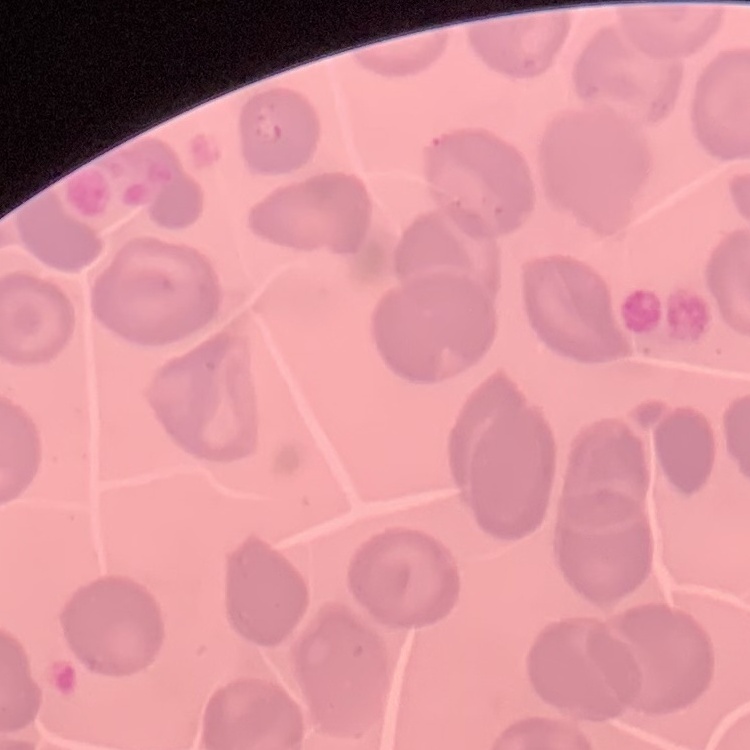 The red blood cells exhibit no rouleaux formation. Thin peripheral smear. Field's or Giemsa stain. Square crop of a larger photomicrograph.